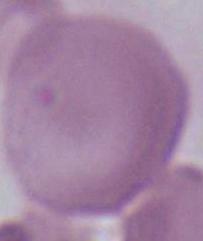
Summary:
  - Identification: red blood cell
  - Magnification: 1000x
  - Modality: photomicrograph